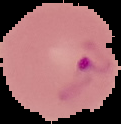 Image is 121×124 pixels. Malaria status: parasitized. From a thin blood film. Segmented cell region on a black background.